Assess the morphology of the erythrocytes.
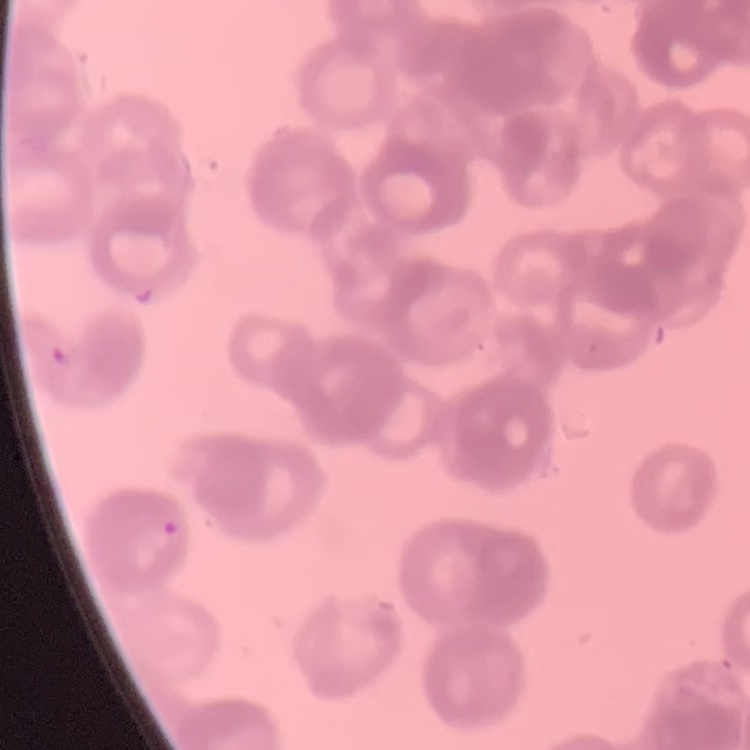
They show rouleaux formation.

One tile cut from a larger photomicrograph. Thin peripheral smear. Stained with either Field's or Giemsa.